Assess this cell for malaria.
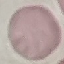
It is uninfected.

Summary:
  - Capture: smartphone through the microscope eyepiece
  - Image type: cell patch, automatically extracted from a larger field of view and resized to 64 × 64 pixels
  - Stain: Giemsa
  - Preparation: thin smear